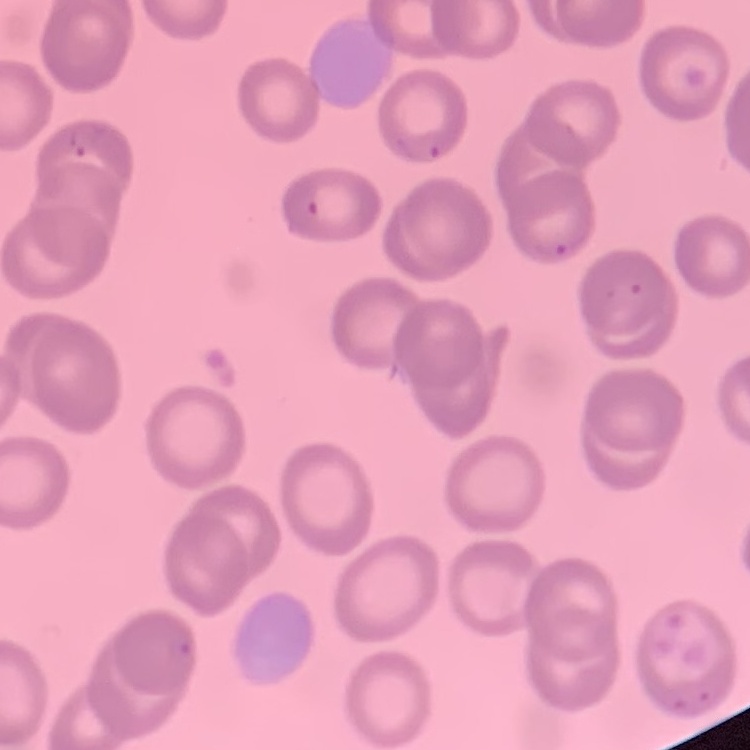

Summary:
  - Erythrocyte morphology: no rouleaux formation
  - Stain: Field's or Giemsa
  - Image type: square crop of a larger photomicrograph
  - Preparation: thin peripheral smear